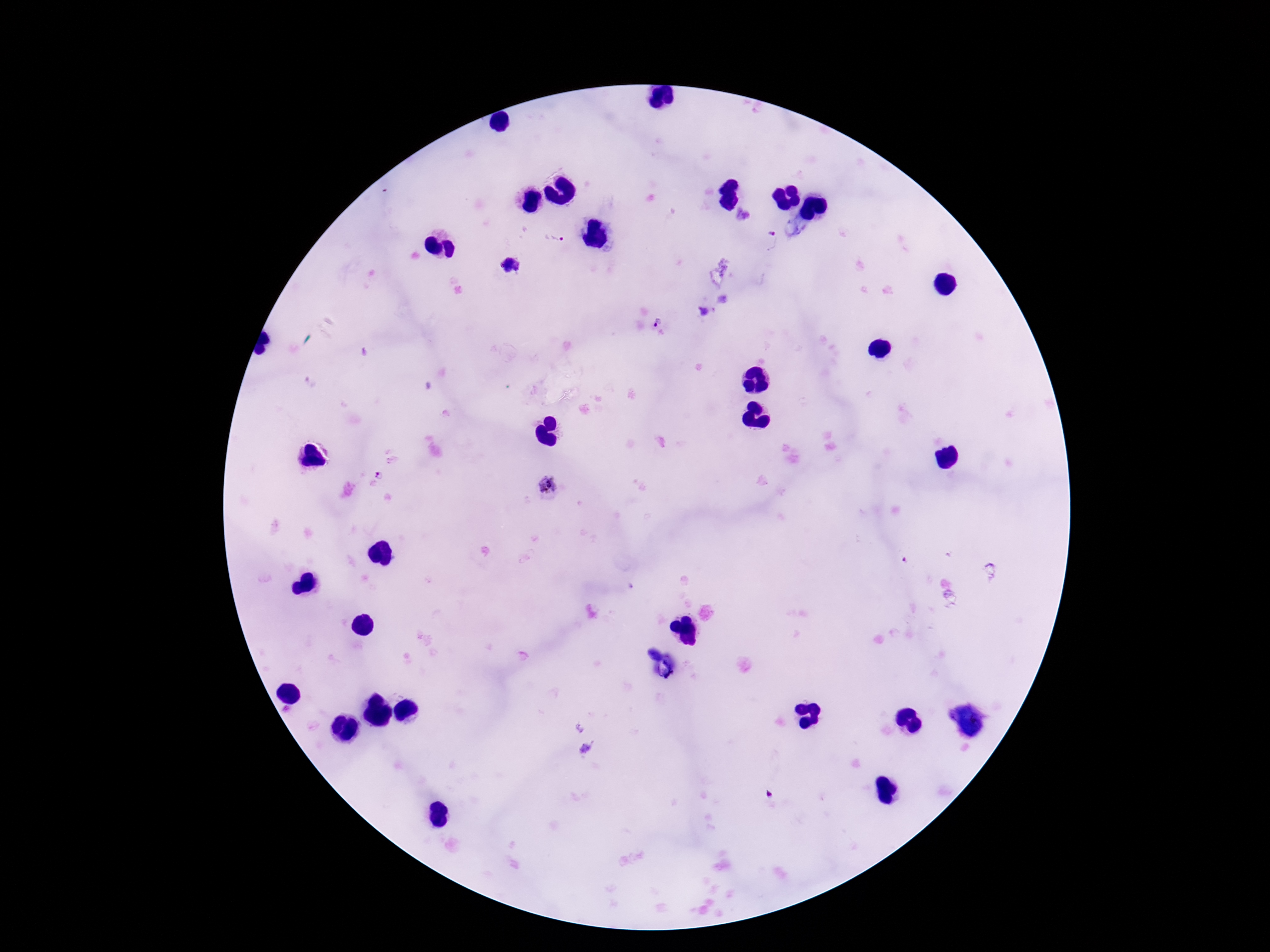
capture: smartphone camera through the microscope eyepiece
field_of_view: one from this slide
stain: Giemsa
magnification: 100x
plasmodium_parasite_locations: 'approximate centers as [x, y] in pixels: [553, 237], [771, 239], [511, 266], [701, 310], [658, 321], [380, 476], [549, 485]'
image_size: 1270×952 pixels
patient_malaria_status: infected
preparation: thick peripheral-blood smear